Classify this cell by malaria status.
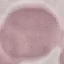
It is uninfected.

Automatically extracted cell patch, resized to 64 × 64 pixels. Acquired by smartphone through the microscope eyepiece. Giemsa-stained preparation. Thin blood smear.